Identify the cell.
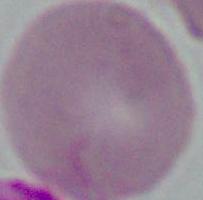
An erythrocyte.

modality: photomicrograph
magnification: 1000x